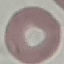 Result: no malaria parasites detected. Thin smear of blood. Acquired by smartphone through the microscope eyepiece. Giemsa stain. Cell patch, automatically extracted from a larger field of view and resized to 64 × 64 pixels.